Identify the parasite.
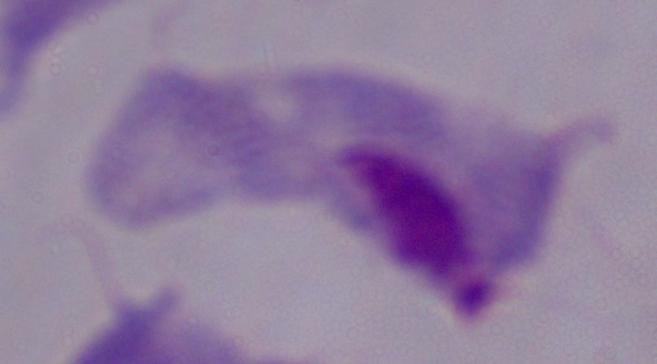

A trichomonad.

modality = photomicrograph
magnification = 1000x